Look for parasitized red blood cells.
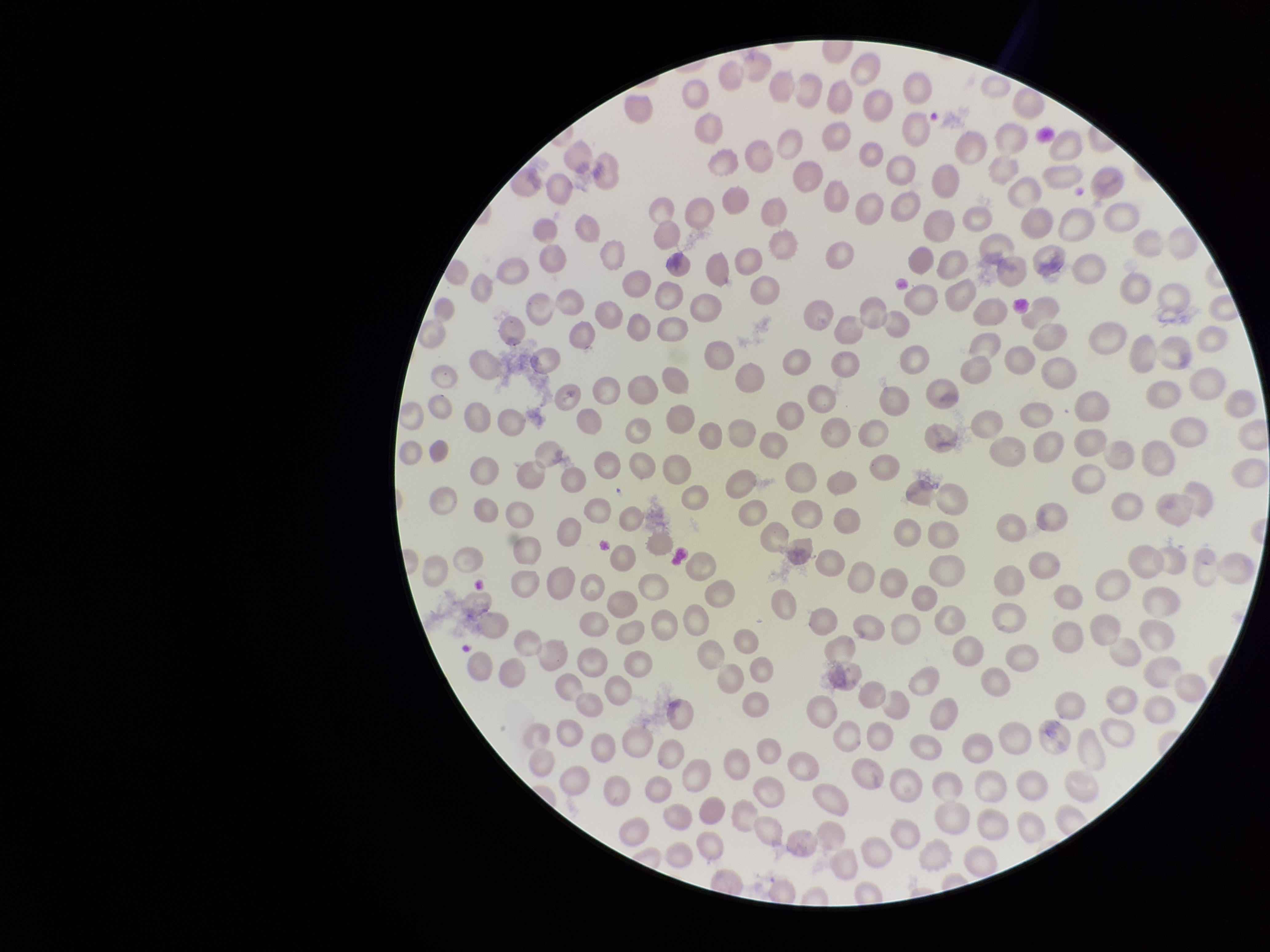
None identified.

Photographed through the microscope eyepiece with a smartphone camera. Single field of view. Image is 1270×952 pixels. Patient malaria status: infected. Red blood cell count: 255. Stained with Giemsa. Parasitized red blood cell count: 0. Species reported for this patient: Plasmodium falciparum. Preparation: thin.